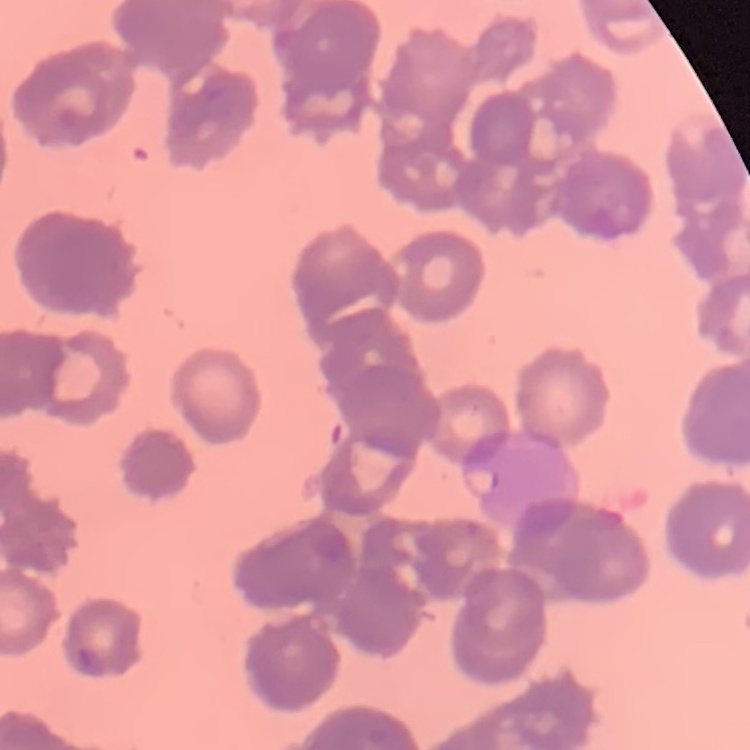

Summary:
  - Erythrocyte morphology: rouleaux formation
  - Image type: square crop of a larger photomicrograph
  - Stain: Field's or Giemsa
  - Preparation: thin peripheral smear